Assess this cell for malaria.
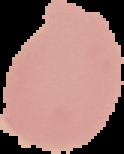
Uninfected.

{
  "preparation": "thin blood smear",
  "image_size": "124×154 pixels",
  "image_type": "segmented cell region with the area outside set to black"
}